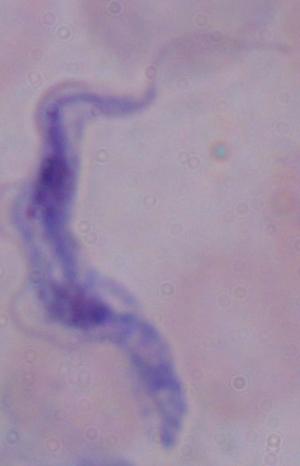

Micrograph. A trypanosome is seen. Captured at 1000x magnification.